Name the blood parasite species.
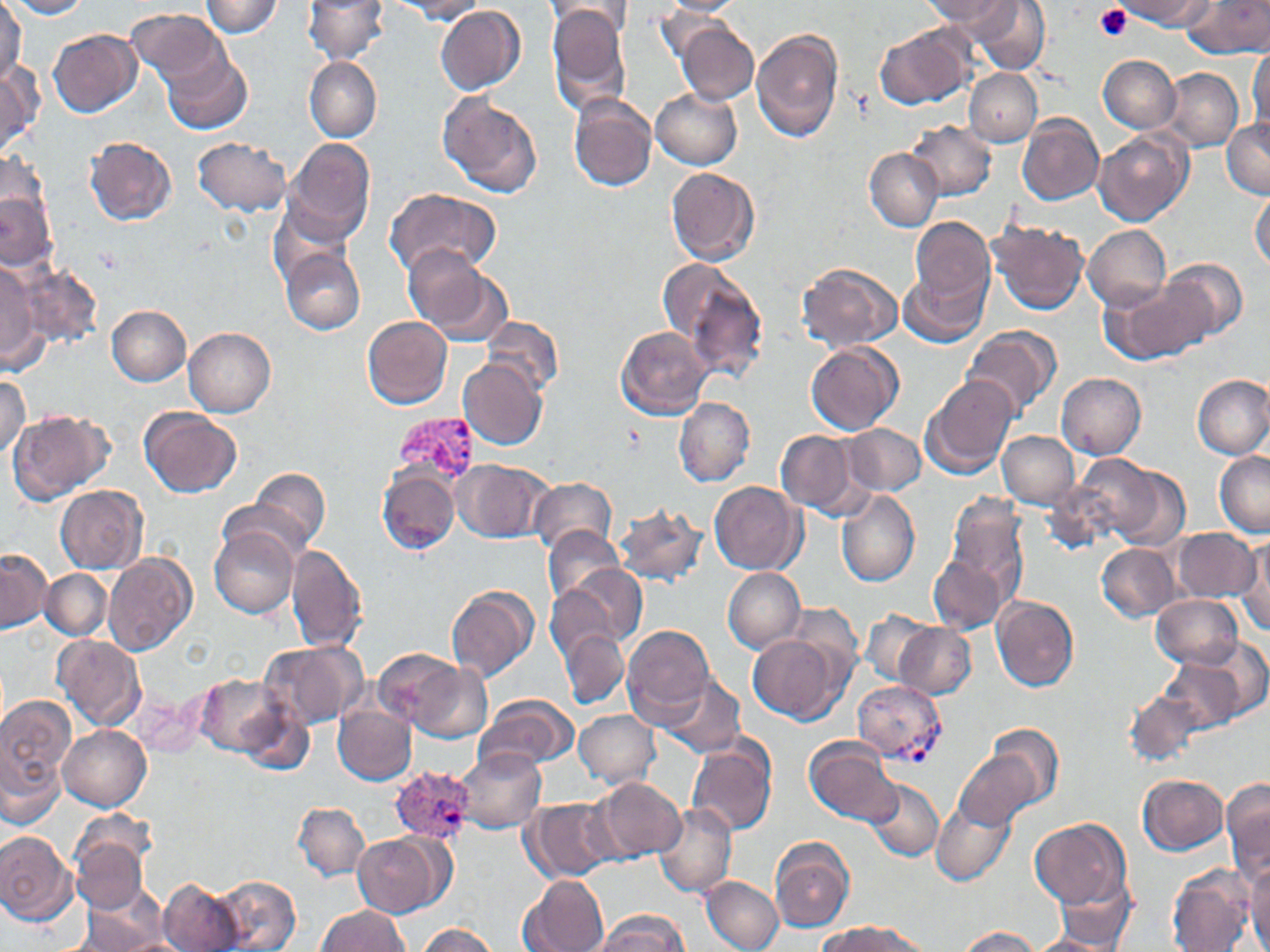

Plasmodium vivax.

modality = optical microscopy
stain = May-Grünwald-Giemsa
magnification = 1000x
image size = 1270×952 pixels
Plasmodium vivax-infected red blood cell locations = approximate bounding boxes as (x1, y1, x2, y2) in pixels: (395, 412, 481, 483), (852, 681, 946, 763), (389, 765, 476, 845)
platelet locations = approximate bounding boxes as (x1, y1, x2, y2) in pixels: (1094, 4, 1132, 41)
field of view = one of a larger specimen
uninfected red blood cell locations = approximate bounding boxes as (x1, y1, x2, y2) in pixels: (8, 0, 89, 18), (200, 0, 282, 37), (303, 0, 387, 64), (392, 0, 486, 23), (547, 0, 631, 44), (656, 0, 747, 16), (973, 0, 1049, 74), (1121, 0, 1213, 29), (1184, 0, 1270, 57), (0, 1, 25, 86), (928, 1, 1014, 32), (547, 6, 631, 114), (435, 7, 525, 95), (126, 8, 227, 86), (674, 21, 758, 105), (875, 25, 972, 108), (750, 27, 844, 143), (49, 29, 142, 118), (1248, 46, 1270, 132), (162, 50, 251, 135), (1097, 55, 1180, 133), (305, 57, 381, 143), (0, 61, 40, 159), (1161, 67, 1243, 151), (964, 69, 1042, 146), (651, 89, 742, 169), (568, 93, 656, 191), (439, 94, 542, 198), (1018, 115, 1103, 206), (1221, 119, 1270, 198), (906, 120, 996, 200), (1094, 131, 1192, 225), (85, 137, 176, 226), (192, 137, 290, 216), (284, 138, 375, 241), (865, 147, 943, 231), (1, 153, 50, 239), (665, 168, 761, 267), (384, 188, 500, 280), (1250, 189, 1270, 270), (0, 193, 55, 271), (268, 203, 352, 287), (909, 216, 995, 306), (988, 221, 1089, 315), (1083, 225, 1170, 310), (402, 245, 498, 338), (279, 248, 365, 335), (1160, 257, 1248, 341), (798, 262, 903, 352), (0, 263, 44, 372), (14, 263, 102, 347), (666, 263, 767, 379), (901, 265, 990, 346), (1101, 282, 1207, 364), (106, 305, 191, 386), (362, 315, 452, 409), (482, 315, 562, 398), (960, 326, 1061, 419), (184, 327, 276, 417), (616, 327, 713, 419), (805, 343, 903, 435), (457, 360, 547, 450), (1057, 372, 1146, 461), (1193, 374, 1270, 459), (0, 375, 30, 458), (921, 375, 1019, 479), (674, 397, 754, 486), (137, 408, 241, 497), (8, 409, 113, 503), (842, 422, 926, 496), (774, 429, 863, 515), (996, 431, 1080, 508), (1214, 450, 1270, 538), (1073, 455, 1182, 549), (453, 460, 554, 543), (377, 467, 460, 554), (248, 468, 331, 548), (529, 478, 618, 556), (709, 482, 805, 575), (57, 486, 147, 573), (836, 489, 920, 588), (942, 495, 1030, 602), (613, 502, 708, 586), (544, 525, 625, 606), (211, 526, 298, 618), (1171, 528, 1261, 603), (1236, 537, 1269, 636), (286, 544, 368, 652), (1097, 544, 1180, 621), (0, 550, 49, 633), (103, 553, 197, 657), (928, 557, 1007, 634), (557, 566, 646, 651), (722, 566, 806, 653), (40, 569, 112, 640), (446, 585, 538, 682), (1151, 595, 1245, 669), (991, 596, 1080, 691), (785, 602, 862, 678), (861, 609, 933, 686), (895, 623, 975, 700), (624, 624, 716, 723), (560, 631, 628, 708), (747, 634, 848, 725), (53, 635, 146, 730), (258, 641, 364, 729), (373, 648, 465, 728), (1162, 648, 1256, 731), (409, 661, 492, 743), (195, 673, 291, 755), (659, 675, 747, 758), (132, 690, 206, 758), (1122, 690, 1207, 767), (0, 693, 74, 807), (475, 694, 579, 770), (235, 701, 314, 775), (333, 702, 417, 786), (574, 709, 659, 789), (987, 723, 1064, 806), (59, 724, 151, 811), (687, 737, 777, 836), (805, 739, 900, 826), (455, 749, 547, 833), (954, 751, 1041, 831), (1137, 774, 1228, 854), (864, 777, 944, 864), (594, 778, 686, 860), (1222, 779, 1270, 882), (521, 797, 617, 882), (293, 801, 371, 881), (653, 801, 737, 899), (931, 801, 1016, 886), (1030, 817, 1131, 912), (70, 826, 150, 913), (0, 831, 77, 924), (354, 833, 449, 917), (771, 839, 855, 933), (1244, 861, 1270, 951), (1167, 864, 1255, 952), (1053, 872, 1136, 949), (518, 874, 609, 952), (208, 875, 300, 951), (700, 876, 783, 952), (158, 877, 246, 951), (77, 886, 169, 951), (317, 906, 409, 952), (593, 910, 688, 952), (823, 921, 927, 952), (419, 923, 498, 952), (957, 927, 1042, 952), (1029, 935, 1119, 952)
preparation = thin blood smear